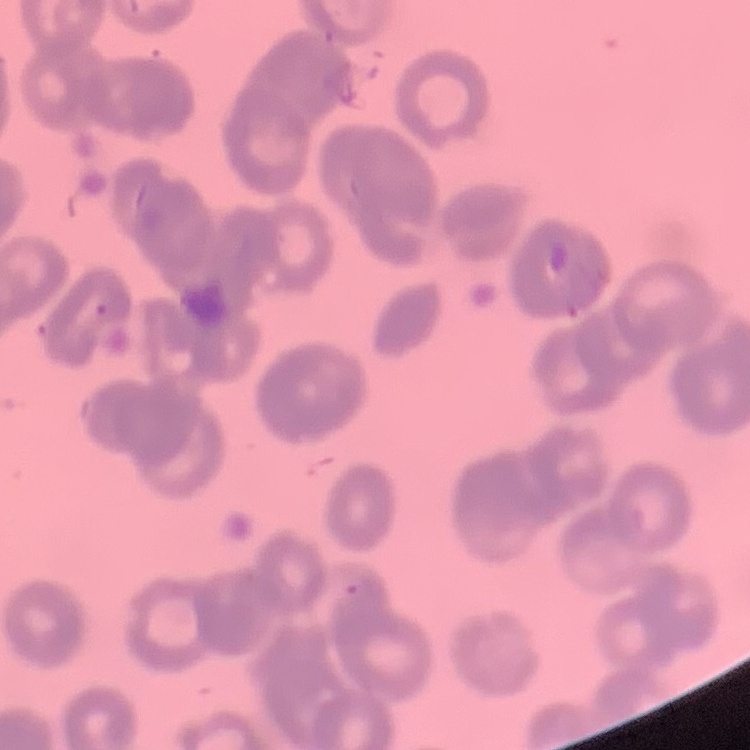
Summary:
  - Erythrocyte morphology: rouleaux formation
  - Preparation: thin blood film
  - Stain: Field's or Giemsa
  - Image type: one tile cut from a larger photomicrograph